Locate every blood parasite and identify its species.
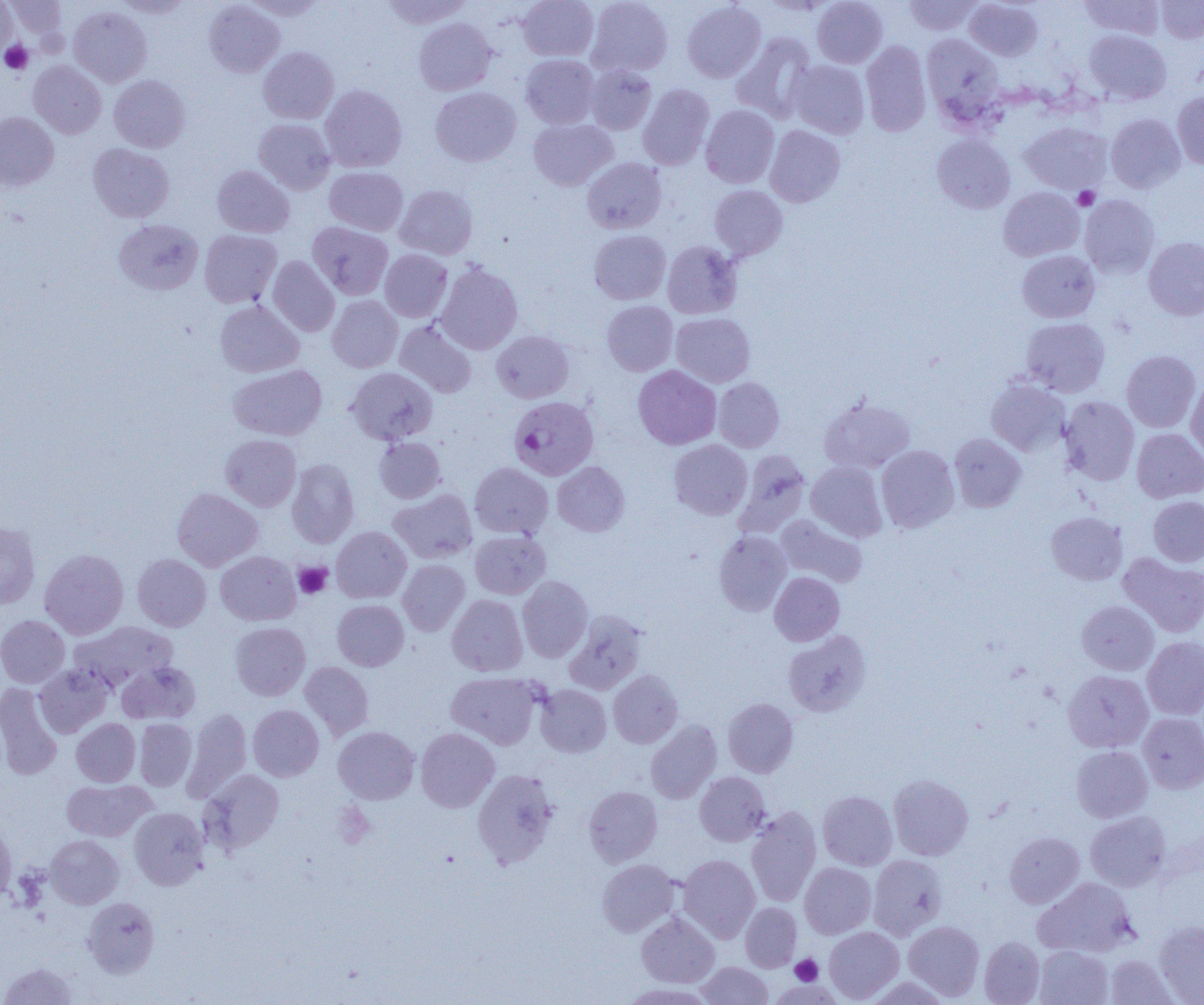
Approximate bounding boxes as (x1,y1)-(x2,y2) corner pairs in pixels.
Plasmodium falciparum-infected red blood cells: (506,396)-(602,485).
No Plasmodium ovale, Plasmodium malariae, Plasmodium vivax, Babesia divergens, or Trypanosoma brucei observed.

Summary:
  - Uninfected red blood cell locations: (5,0)-(67,39), (114,0)-(194,18), (243,0)-(327,20), (381,0)-(472,28), (518,0)-(599,61), (586,0)-(673,77), (812,0)-(888,68), (903,0)-(984,35), (1079,0)-(1164,39), (1156,0)-(1204,44), (204,1)-(284,78), (682,1)-(766,83), (964,1)-(1043,61), (0,2)-(18,59), (68,5)-(152,87), (414,18)-(497,95), (1084,29)-(1171,105), (731,32)-(817,123), (921,33)-(1004,123), (861,41)-(931,137), (258,47)-(339,124), (521,54)-(599,128), (28,60)-(106,139), (787,60)-(869,139), (585,65)-(657,134), (109,75)-(190,152), (637,84)-(715,170), (319,85)-(408,172), (430,87)-(521,166), (1172,91)-(1204,169), (701,104)-(779,188), (0,111)-(59,190), (1106,113)-(1186,193), (253,118)-(335,194), (528,118)-(617,190), (1019,122)-(1112,194), (765,125)-(845,207), (931,134)-(1015,214), (87,143)-(175,222), (582,157)-(666,234), (212,165)-(294,238), (324,166)-(408,236), (394,184)-(478,260), (709,185)-(787,260), (998,187)-(1083,261), (1079,195)-(1160,279), (114,219)-(203,295), (307,222)-(393,300), (199,230)-(282,308), (589,230)-(671,304), (1143,237)-(1204,320), (662,241)-(742,318), (380,249)-(452,322), (1017,250)-(1100,323), (267,256)-(340,337), (436,262)-(523,354), (327,295)-(403,372), (214,300)-(304,377), (602,300)-(678,376), (671,313)-(755,387), (1020,317)-(1110,397), (395,319)-(477,398), (491,330)-(574,403), (1121,350)-(1201,432), (228,364)-(327,440), (633,365)-(721,449), (345,367)-(438,445), (1186,376)-(1204,463), (714,377)-(785,452), (986,377)-(1071,455), (819,396)-(916,473), (1059,396)-(1139,485), (1132,428)-(1204,503), (949,433)-(1026,512), (220,434)-(301,511), (374,437)-(446,503), (669,440)-(753,520), (876,445)-(959,532), (733,450)-(811,538), (286,458)-(359,548), (806,461)-(888,542), (552,462)-(630,536), (470,463)-(553,539), (172,488)-(263,571), (389,489)-(477,563), (1148,496)-(1204,566), (1046,512)-(1127,585), (776,514)-(868,587), (0,520)-(41,609), (331,526)-(411,603), (470,531)-(550,599), (713,531)-(791,616), (40,549)-(128,639), (215,551)-(301,625), (1118,552)-(1204,638), (132,554)-(211,631), (397,559)-(470,635), (769,571)-(844,646), (517,576)-(593,662), (447,595)-(528,676), (332,599)-(408,670), (1076,600)-(1159,675), (564,610)-(647,694), (0,615)-(70,688), (69,622)-(178,693), (231,622)-(311,700), (783,631)-(871,717), (1142,637)-(1204,719), (117,661)-(201,724), (300,661)-(374,740), (34,664)-(112,737), (1062,669)-(1153,753), (608,670)-(682,748), (446,671)-(543,749), (0,683)-(63,781), (535,684)-(611,757), (723,697)-(798,777), (248,705)-(324,781), (182,708)-(252,802), (1138,713)-(1204,794), (71,718)-(140,786), (134,719)-(196,791), (645,720)-(722,804), (333,726)-(420,804), (415,728)-(499,812), (1072,745)-(1152,822), (472,768)-(560,868), (200,769)-(284,854), (694,771)-(771,846), (889,774)-(973,860), (61,779)-(156,842), (583,786)-(662,867), (818,790)-(897,870), (129,807)-(209,890), (745,807)-(822,906), (1085,811)-(1171,891), (0,822)-(17,903), (1004,832)-(1084,908), (45,834)-(124,909), (678,854)-(760,942), (867,854)-(948,940), (596,859)-(681,937), (799,863)-(876,939), (1032,877)-(1137,957), (82,897)-(159,977), (740,902)-(801,972), (636,912)-(719,987), (904,920)-(985,1000), (1154,920)-(1204,1004), (824,926)-(904,1003), (979,937)-(1045,1004), (1033,945)-(1113,1005), (1105,955)-(1178,1005), (696,961)-(773,1005), (1,962)-(79,1005), (864,977)-(952,1005), (621,982)-(715,1004)
  - Platelet locations: (0,39)-(33,75), (1073,186)-(1100,210), (294,562)-(332,598), (333,803)-(375,849), (790,954)-(823,985)
  - Slide-level diagnosis: Plasmodium falciparum
  - Magnification: 1000x
  - Modality: light microscopy
  - Preparation: thin blood smear
  - Image size: 1204×1005 pixels
  - Field of view: single